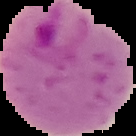

Summary:
  - Image type: segmented cell region with the area outside set to black
  - Preparation: thin blood smear
  - Malaria status: parasitized
  - Image size: 136×136 pixels